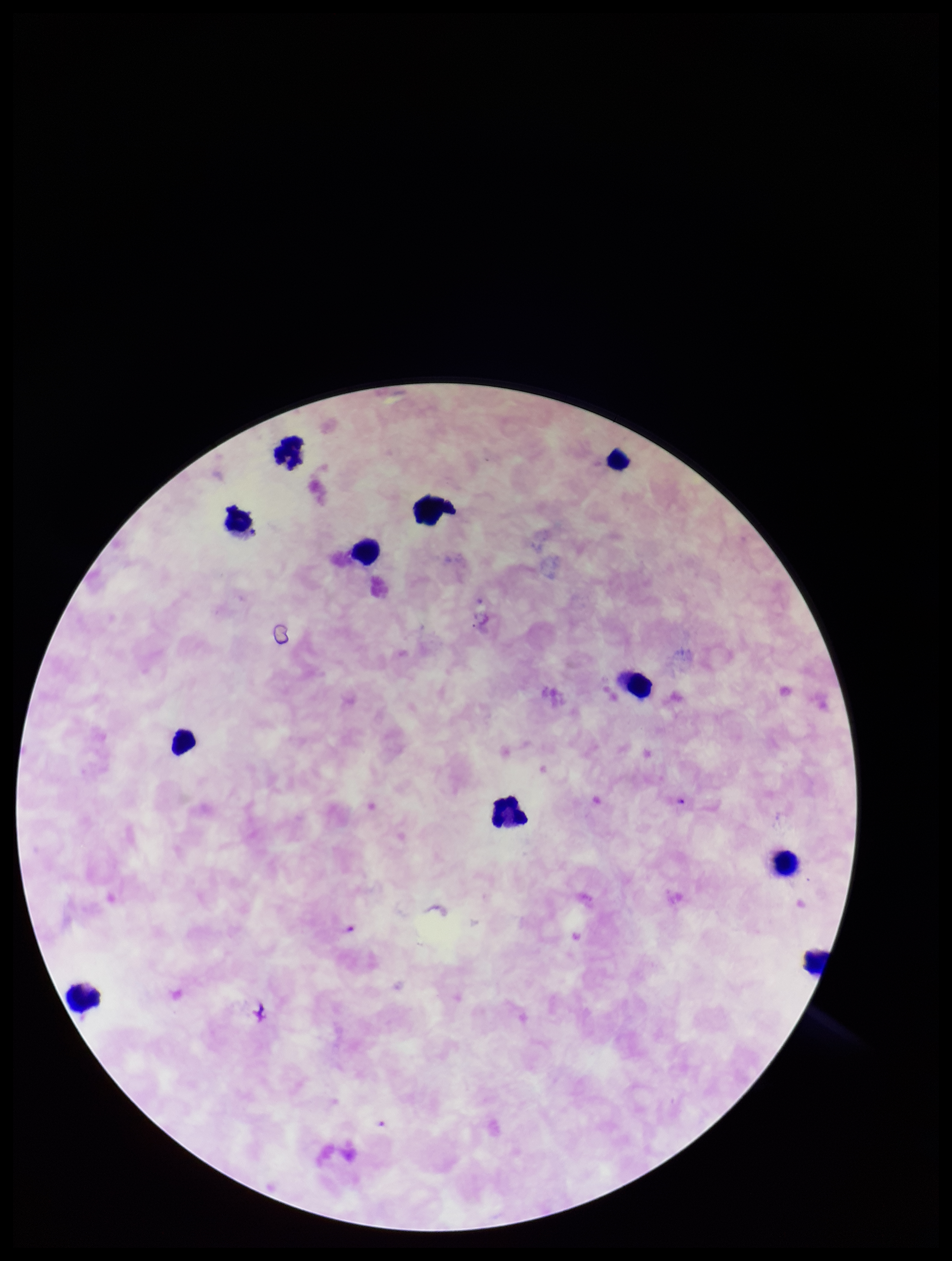
stain = Giemsa
species reported for this patient = Plasmodium falciparum
patient malaria status = positive
image size = 952×1261 pixels
parasite count = 0
Plasmodium parasites = none identified
preparation = thick smear
field of view = single
leukocyte count = 11
capture = smartphone photograph through the microscope eyepiece